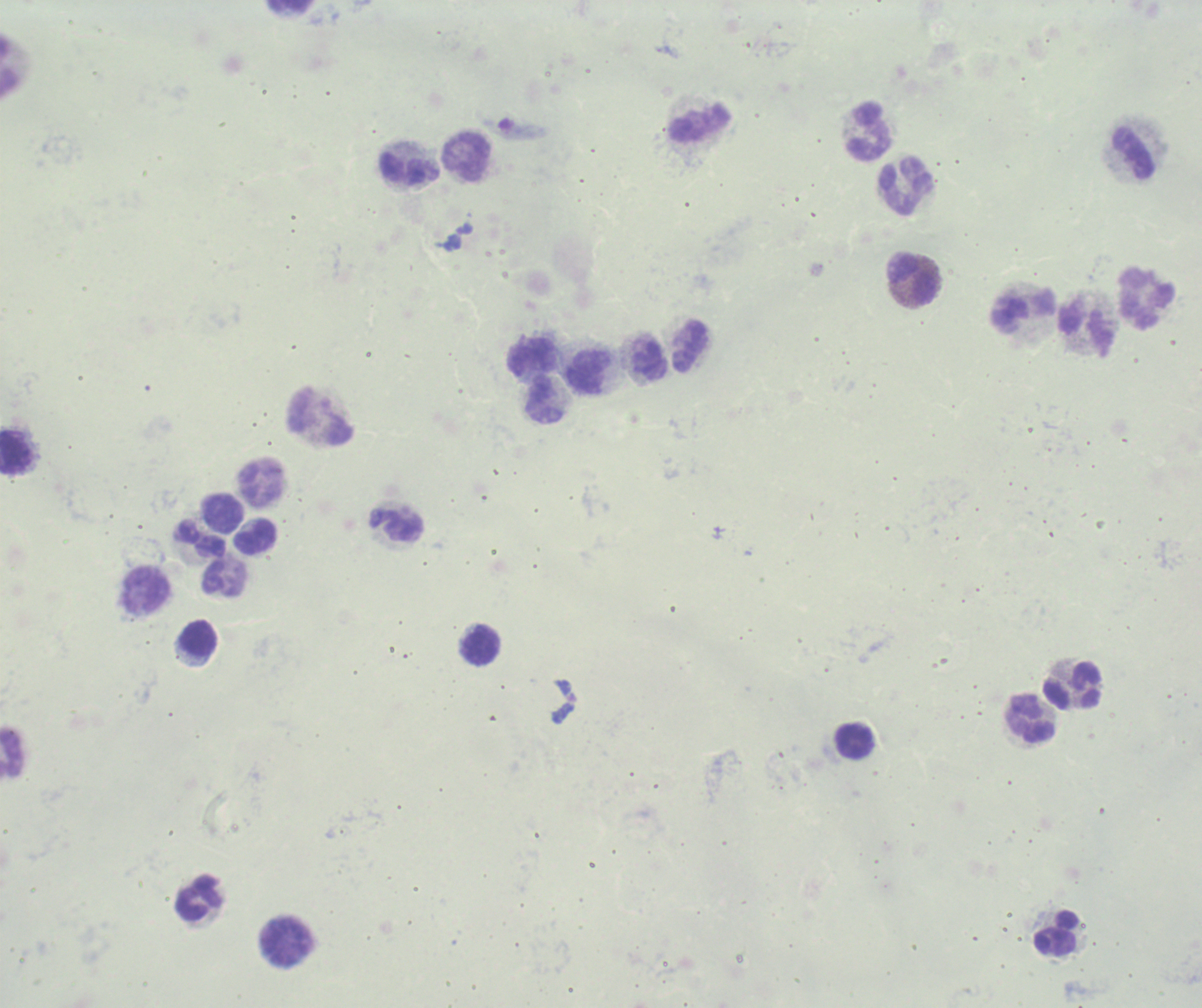

Approximate centers as (x, y) in pixels.
Summary:
  - Leukocyte locations: (699, 123), (870, 131), (1134, 154), (468, 158), (410, 168), (906, 187), (913, 278), (1146, 299), (1025, 313), (1087, 330), (692, 347), (533, 357), (652, 362), (588, 371), (545, 401), (320, 418), (14, 453), (261, 483), (222, 513), (397, 526), (200, 537), (255, 537), (224, 579), (146, 591), (199, 638), (480, 646), (1074, 687), (1029, 719), (854, 741), (12, 754), (199, 899), (1057, 933), (286, 942)
  - Magnification: 100x
  - Field of view: single
  - Context: previously used in a real diagnosis
  - Stain: Romanowsky
  - Result: no malaria parasites detected
  - Image size: 1202×1008 pixels
  - Background quality: unsatisfactory
  - Preparation: thick blood film